Locate and identify every blood parasite.
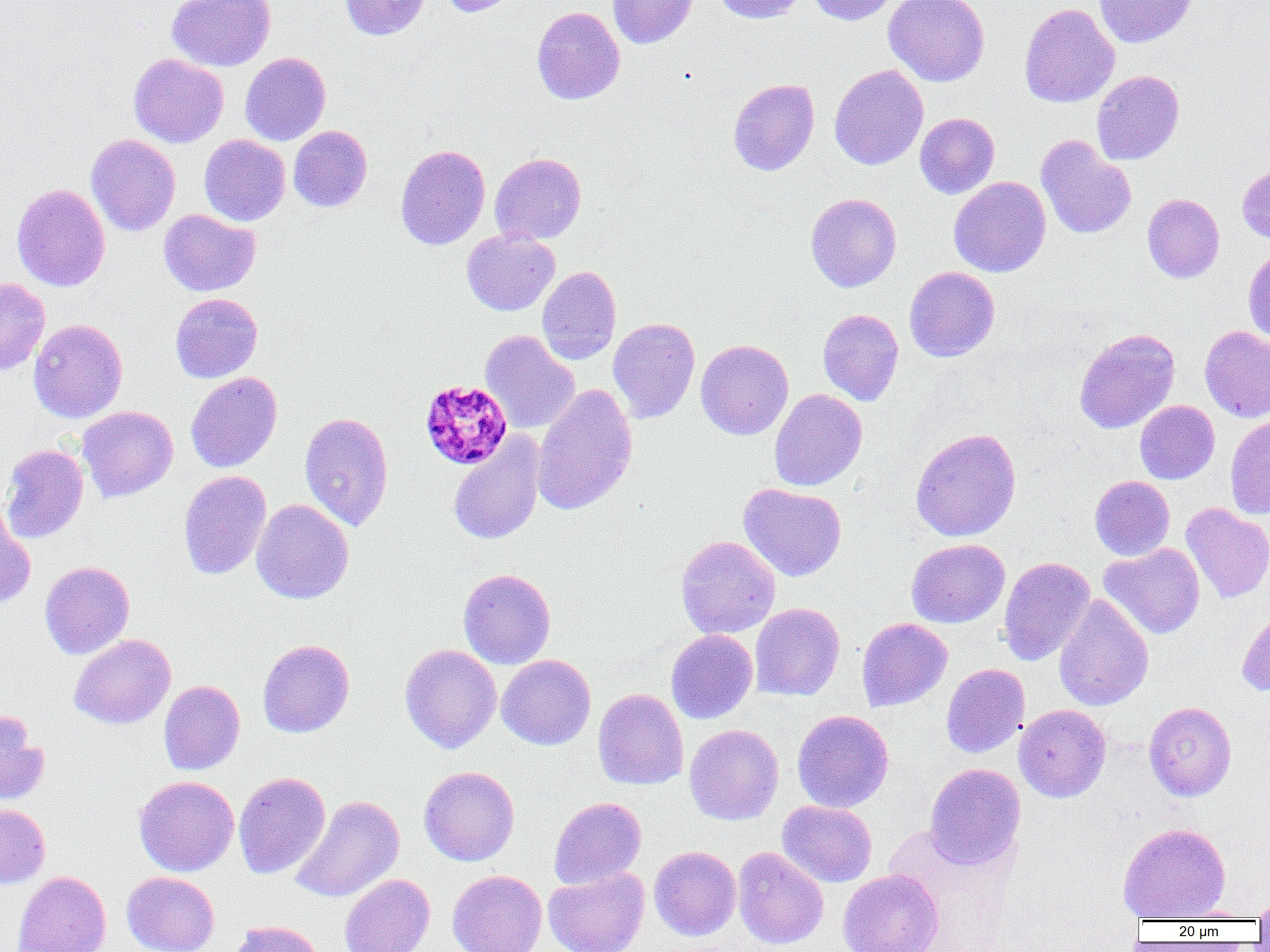

Approximate bounding boxes as (x1,y1)-(x2,y2) corner pairs in pixels.
Plasmodium malariae-infected red blood cells: (419,379)-(513,470).
No Plasmodium falciparum, Plasmodium ovale, Plasmodium vivax, Babesia divergens, or Trypanosoma brucei observed.

Uninfected red blood cell locations: (166,0)-(275,71), (339,0)-(431,40), (439,0)-(520,17), (607,0)-(699,49), (712,0)-(806,24), (807,0)-(900,25), (883,0)-(990,87), (1093,0)-(1198,48), (1019,3)-(1120,107), (531,6)-(625,105), (240,52)-(331,146), (128,53)-(228,148), (829,64)-(929,170), (1092,70)-(1184,165), (728,78)-(820,176), (914,112)-(1000,199), (288,125)-(372,212), (86,134)-(181,236), (199,134)-(290,226), (1035,134)-(1136,239), (395,144)-(490,250), (489,152)-(586,245), (1237,163)-(1270,245), (948,176)-(1051,277), (11,183)-(110,292), (805,193)-(901,292), (1142,193)-(1224,283), (158,209)-(260,296), (461,229)-(560,316), (1242,246)-(1270,344), (537,266)-(621,365), (904,266)-(1000,362), (0,278)-(50,375), (170,292)-(263,383), (817,309)-(904,406), (28,318)-(128,423), (608,318)-(700,423), (1199,325)-(1270,422), (1074,328)-(1180,434), (479,330)-(580,434), (696,339)-(793,440), (185,371)-(282,473), (531,384)-(638,516), (769,389)-(867,491), (1135,400)-(1220,484), (76,406)-(178,502), (299,411)-(394,532), (1224,414)-(1270,519), (910,427)-(1022,542), (448,433)-(545,545), (0,444)-(89,543), (178,470)-(271,580), (1089,475)-(1175,561), (738,483)-(847,582), (251,499)-(354,604), (1181,503)-(1270,603), (0,504)-(36,610), (676,535)-(780,639), (906,538)-(1010,628), (1099,543)-(1205,639), (998,556)-(1095,666), (39,561)-(135,659), (458,568)-(555,669), (1054,593)-(1154,712), (750,602)-(845,701), (1236,602)-(1270,697), (856,617)-(952,711), (666,629)-(757,724), (69,634)-(176,729), (257,639)-(355,738), (399,644)-(502,753), (496,654)-(596,750), (941,663)-(1029,758), (158,680)-(245,775), (593,688)-(689,790), (1144,701)-(1237,801), (1014,704)-(1111,803), (792,710)-(894,812), (0,711)-(49,806), (684,724)-(784,825), (924,763)-(1025,869), (418,766)-(520,866), (233,772)-(331,879), (133,775)-(239,877), (289,795)-(404,903), (548,796)-(646,889), (777,800)-(877,887), (0,804)-(51,888), (1117,823)-(1231,921), (649,846)-(741,940), (732,847)-(829,950), (543,866)-(650,952), (838,869)-(944,952), (447,870)-(547,952), (12,871)-(111,952), (121,872)-(219,952), (339,874)-(435,952), (1252,892)-(1270,924), (1169,906)-(1258,921), (227,920)-(327,952). Slide-level diagnosis: Plasmodium malariae. Image is 1270×952 pixels. One field of a larger specimen. Light microscopy. Thin blood film. 1000x magnification.